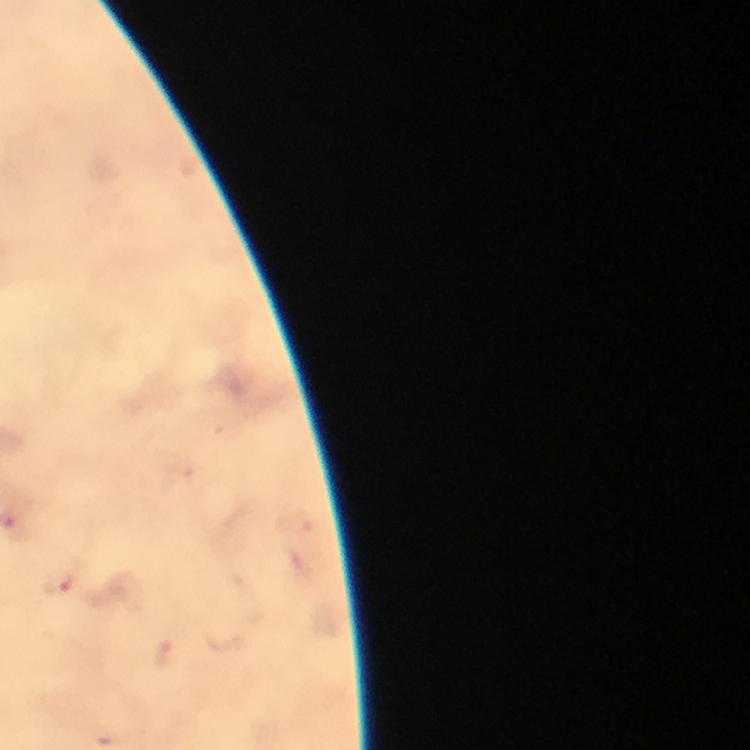

preparation = thick smear
capture = smartphone mounted on the microscope
magnification = 100x
context = from a diagnostic examination for malaria
stain = Giemsa
immersion oil = used
Plasmodium parasite locations = approximate centers as {x, y} in pixels: {59, 585}, {166, 658}
cropped from = a single field of view
image size = 750×750 pixels